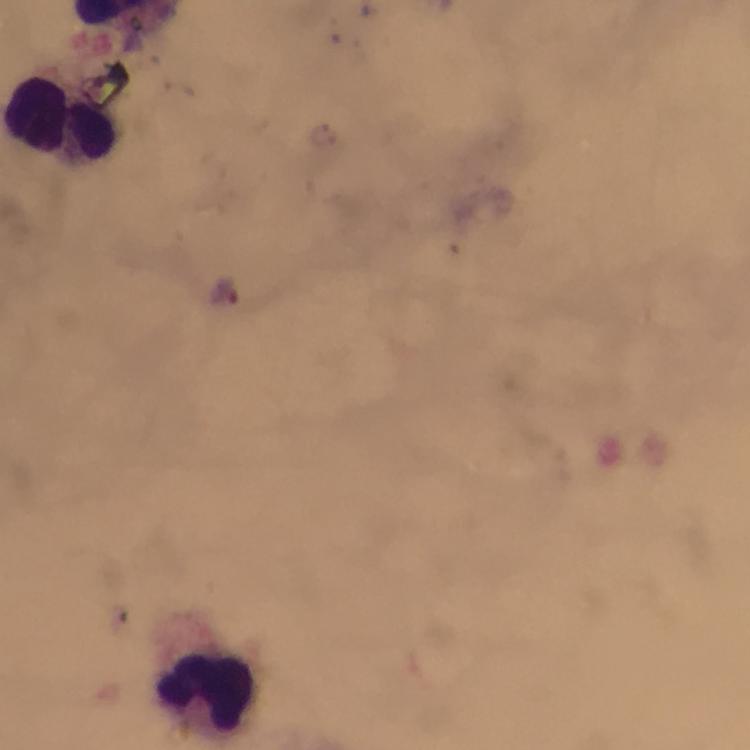
Approximate object centers, in pixels from the top-left corner.
Summary:
  - Plasmodium parasite locations: (x=223, y=291)
  - Leukocyte locations: (x=61, y=124), (x=206, y=691)
  - Cropped from: one field of view
  - Stain: Giemsa
  - Context: from a malaria diagnostic workup
  - Immersion oil: used
  - Image size: 750×750 pixels
  - Magnification: 100x
  - Capture: smartphone mounted on the microscope
  - Preparation: thick smear